Report the malaria status.
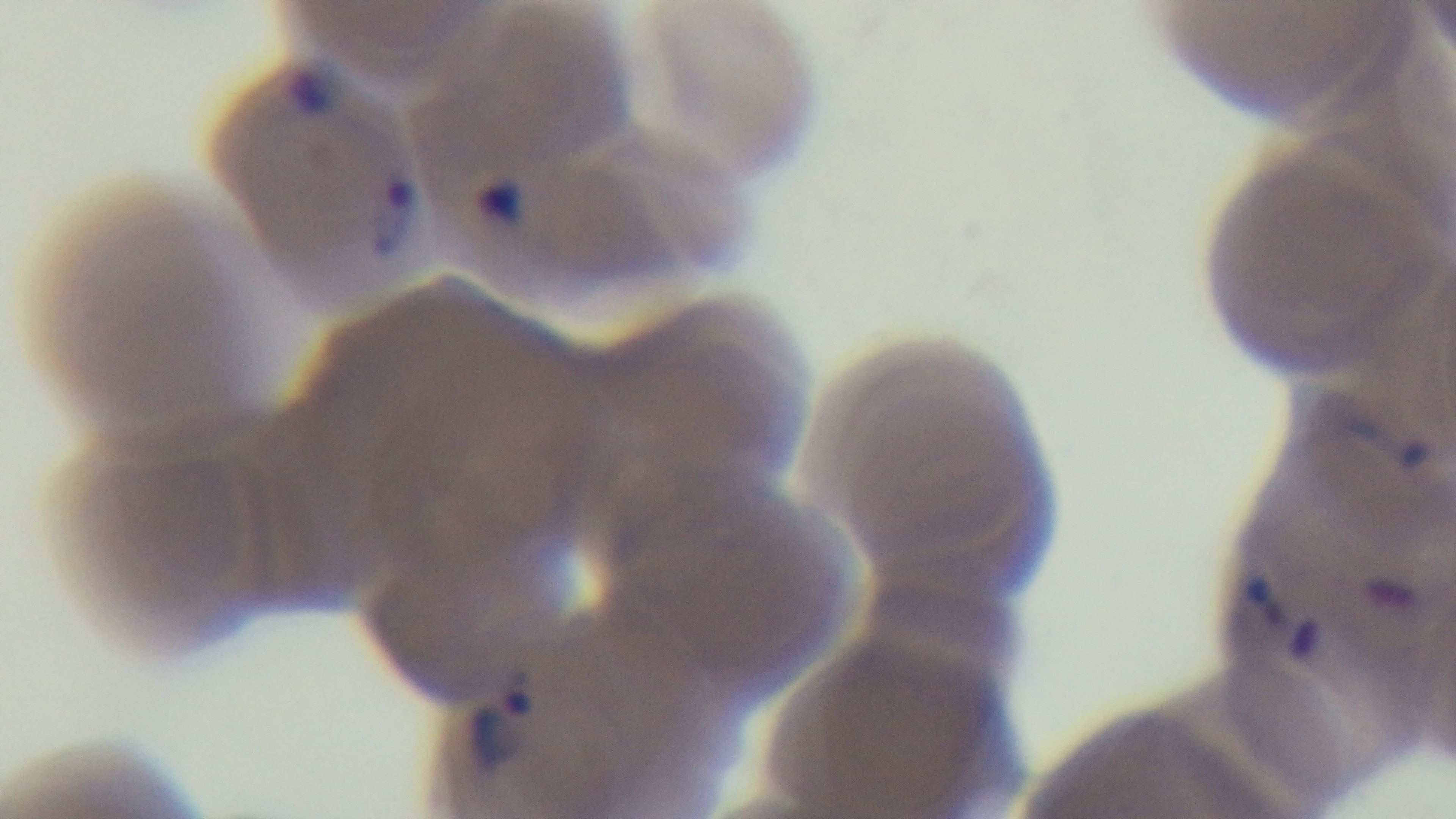

Positive.

Preparation: thin smear. Photomicrograph. Giemsa-stained. Mounted 4K digital camera. Oil-immersion objective, 100x. One field from the slide.